Draw a bounding box around every trophozoite.
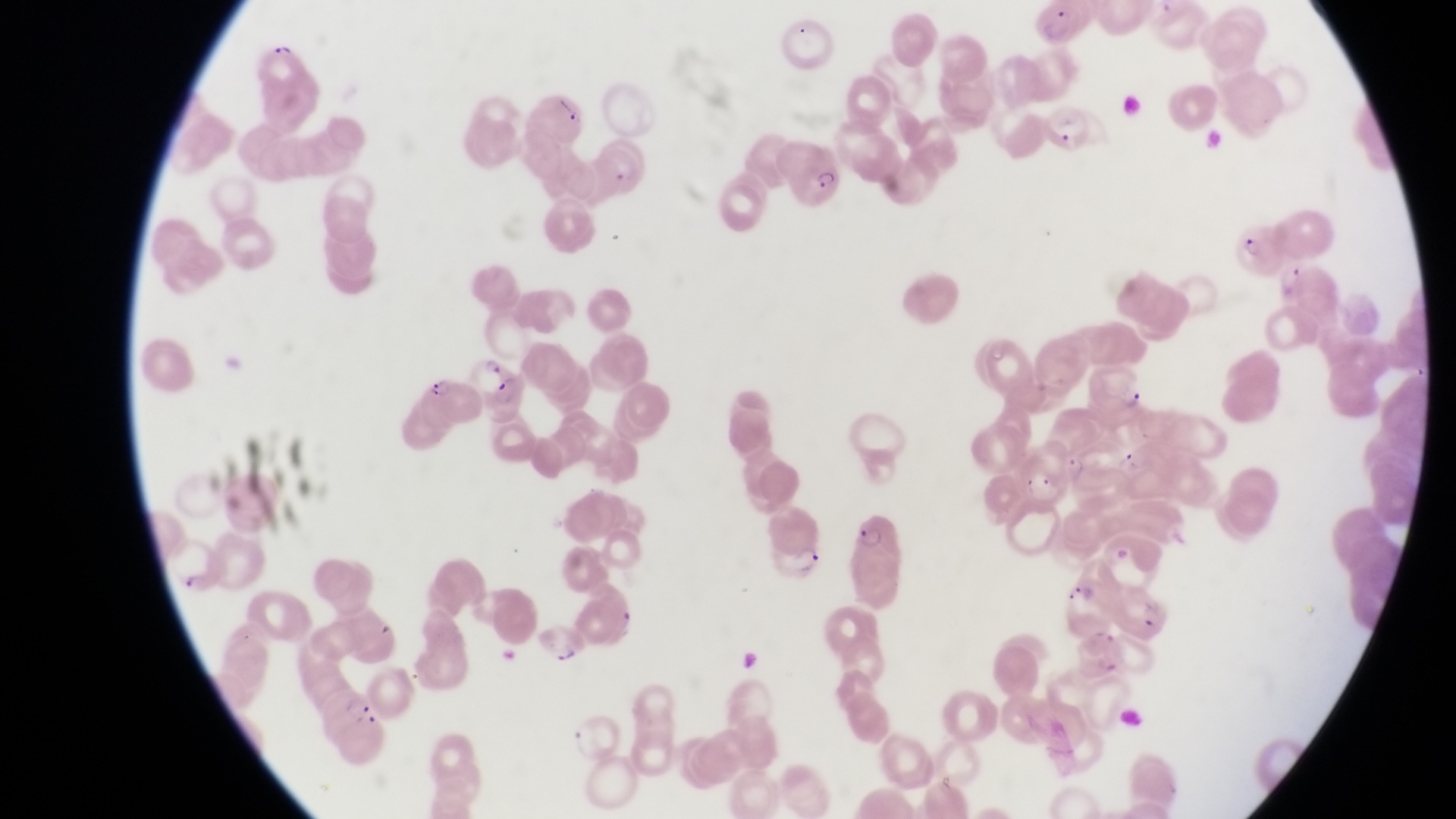
Approximate bounding boxes as {left, top, right, bottom} in pixels.
Trophozoites: {478, 347, 504, 374}, {1118, 384, 1147, 410}, {551, 640, 581, 669}.

country: Uganda
artifact_platelet_like_body_stain_precipitate_or_debris_locations: 'approximate bounding boxes as {left, top, right, bottom} in pixels: {267, 37, 294, 58}, {552, 93, 578, 126}'
magnification: 1000x
preparation: thin blood smear
parasitised_red_blood_cell_locations: 'approximate bounding boxes as {left, top, right, bottom} in pixels: {1038, 4, 1087, 52}, {1036, 98, 1083, 147}, {783, 140, 844, 209}, {1237, 218, 1292, 277}, {423, 362, 482, 423}, {488, 373, 534, 428}, {838, 507, 914, 612}, {766, 508, 833, 581}, {324, 692, 381, 745}'
capture: smartphone photograph through the eyepiece of an Olympus CX-23 microscope
image_size: 1456×819 pixels
field_of_view: single